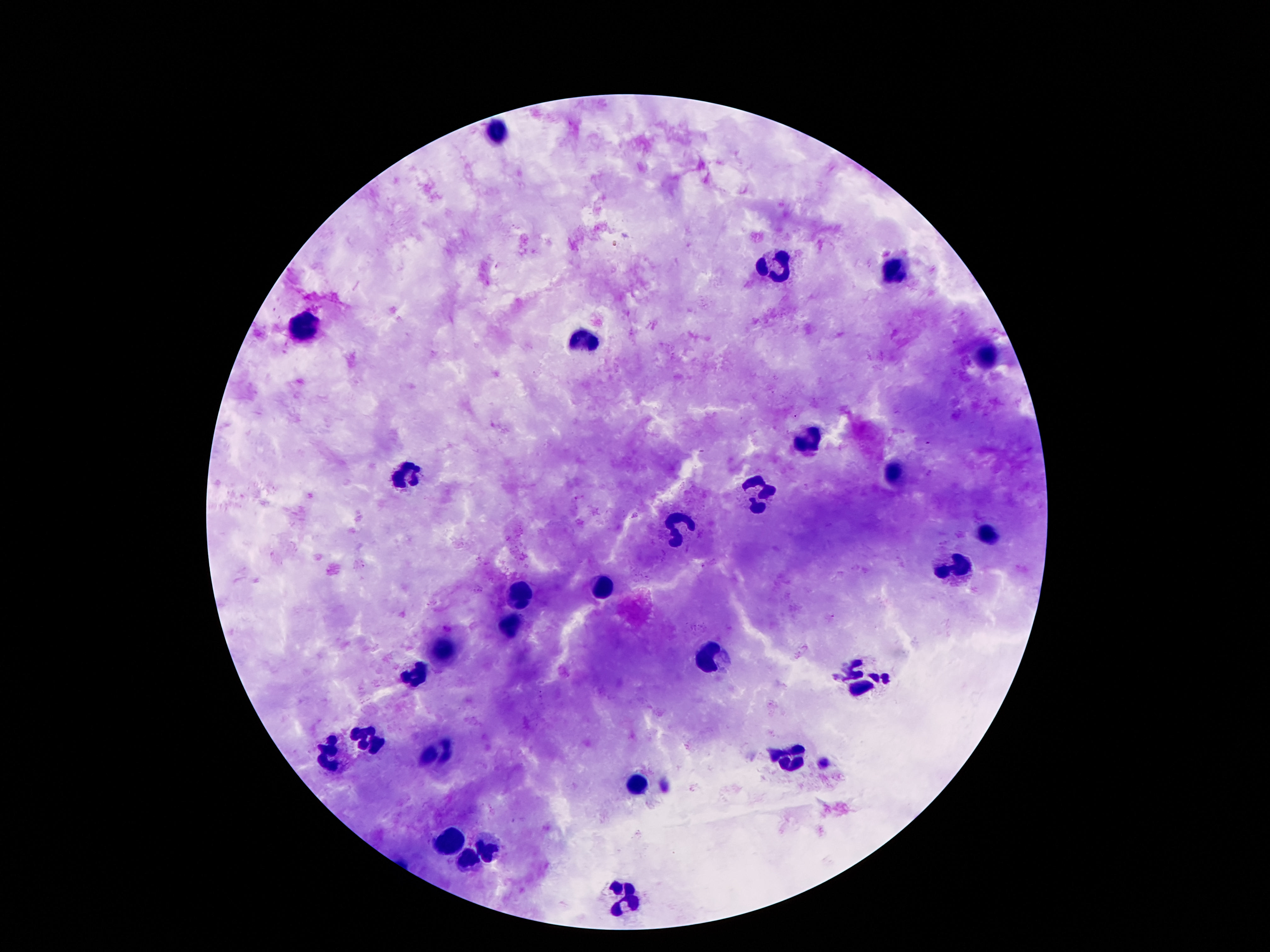
leukocyte locations = approximate object centers, in pixels from the top-left corner: (x=497, y=134), (x=780, y=265), (x=895, y=271), (x=303, y=325), (x=584, y=338), (x=984, y=356), (x=807, y=437), (x=407, y=473), (x=891, y=475), (x=756, y=490), (x=681, y=528), (x=988, y=535), (x=953, y=565), (x=606, y=583), (x=520, y=597), (x=511, y=625), (x=442, y=650), (x=709, y=661), (x=413, y=674), (x=867, y=676), (x=369, y=739), (x=327, y=752), (x=436, y=754), (x=791, y=756), (x=643, y=787), (x=449, y=843), (x=489, y=849), (x=467, y=860), (x=625, y=895)
patient malaria status = uninfected
magnification = 100x
stain = Giemsa
image size = 1270×952 pixels
preparation = thick peripheral-blood smear
capture = smartphone camera through the microscope eyepiece
field of view = one from this slide